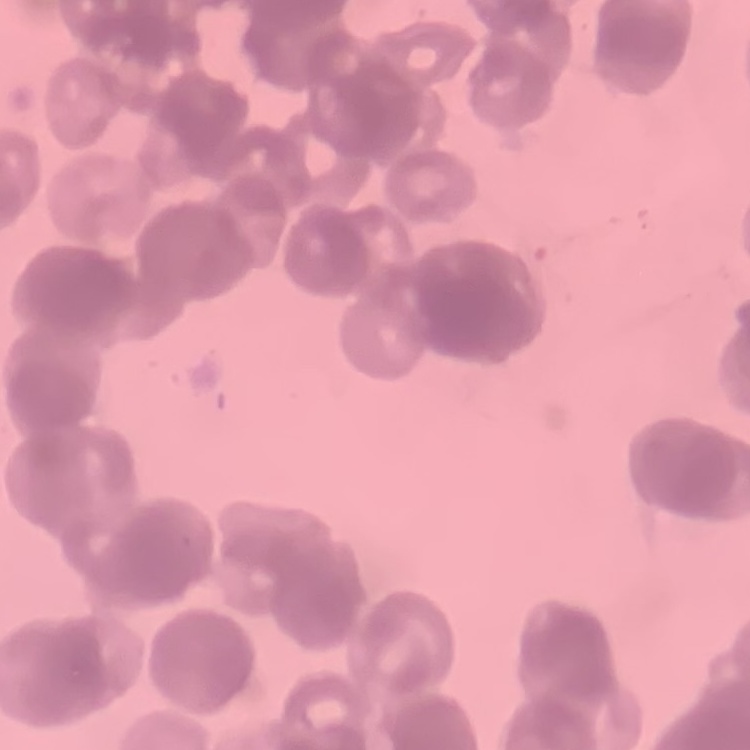
The erythrocytes exhibit rouleaux formation. One tile cut from a larger photomicrograph. Thin blood smear. Stained with either Field's or Giemsa.